Locate every blood parasite and identify its species.
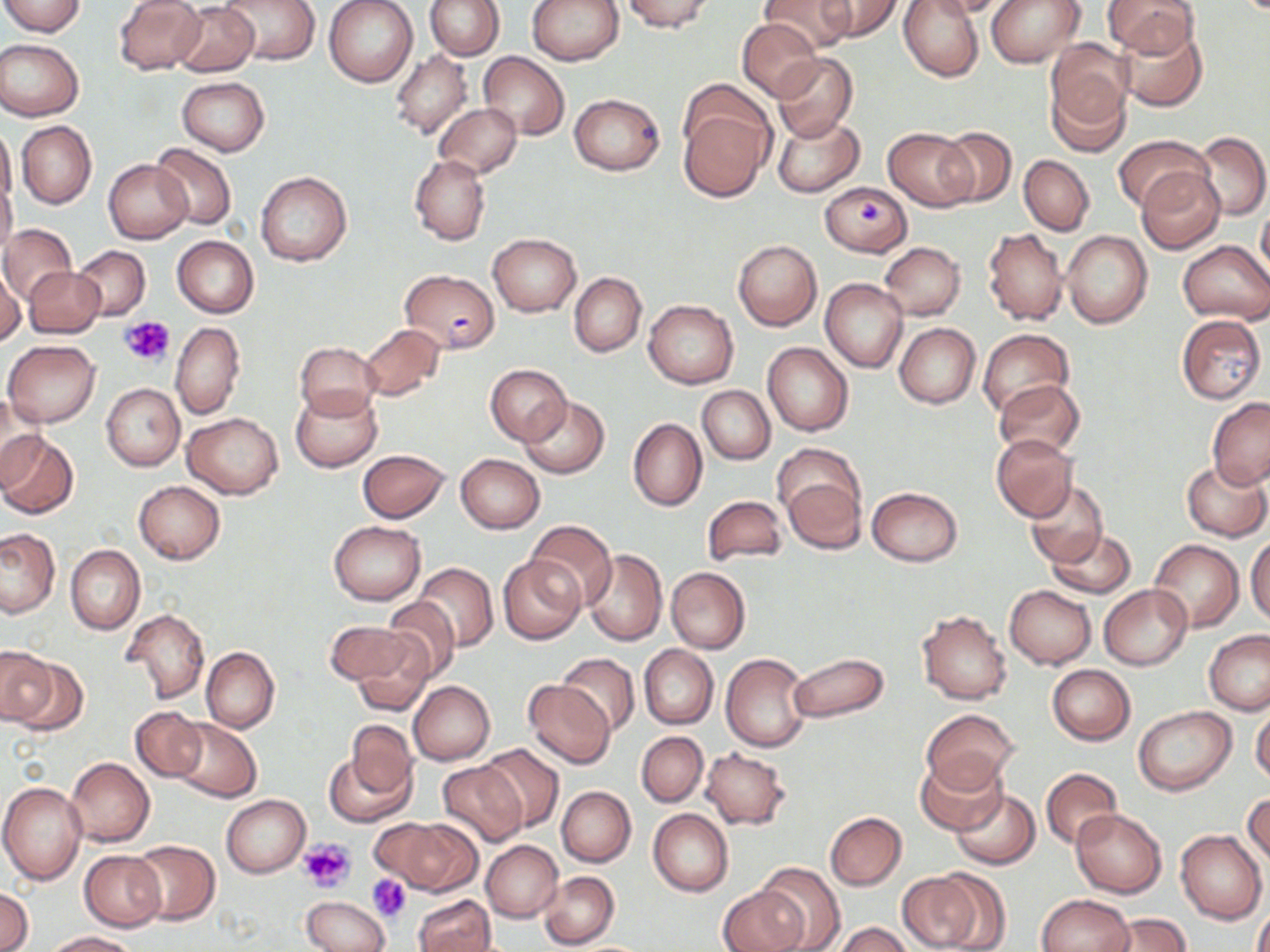

Approximate bounding boxes as (x1, y1, x2, y2) in pixels.
Plasmodium falciparum-infected red blood cells: (400, 269, 500, 354).
No Plasmodium ovale, Plasmodium malariae, Plasmodium vivax, Babesia divergens, or Trypanosoma brucei observed.

Summary:
  - Uninfected red blood cell locations: (2, 0, 86, 36), (219, 0, 321, 65), (324, 0, 418, 87), (425, 0, 504, 60), (527, 0, 624, 65), (621, 0, 715, 33), (758, 0, 857, 55), (817, 0, 902, 42), (898, 0, 985, 81), (923, 0, 1013, 19), (986, 0, 1085, 67), (1104, 0, 1201, 58), (113, 1, 206, 74), (171, 2, 260, 76), (738, 18, 824, 102), (1115, 21, 1207, 111), (0, 39, 83, 121), (1044, 39, 1134, 143), (391, 49, 473, 139), (479, 52, 569, 137), (773, 53, 857, 143), (178, 78, 269, 155), (568, 93, 665, 175), (436, 103, 520, 178), (679, 107, 772, 203), (772, 114, 864, 197), (16, 120, 96, 209), (0, 122, 17, 209), (937, 127, 1016, 206), (885, 128, 976, 210), (1194, 132, 1270, 221), (1113, 134, 1209, 212), (150, 143, 236, 229), (409, 154, 490, 246), (1019, 155, 1094, 235), (104, 160, 191, 244), (1136, 166, 1226, 254), (255, 171, 353, 267), (1, 177, 18, 260), (820, 180, 912, 255), (1258, 204, 1270, 282), (0, 224, 75, 305), (983, 227, 1068, 326), (1061, 231, 1153, 329), (487, 234, 582, 316), (171, 236, 259, 317), (732, 240, 822, 330), (1178, 241, 1270, 323), (880, 242, 965, 320), (72, 246, 150, 318), (1, 265, 25, 344), (25, 267, 104, 337), (569, 273, 646, 356), (820, 279, 908, 372), (644, 299, 739, 388), (1177, 315, 1266, 403), (171, 322, 244, 420), (894, 322, 980, 408), (359, 324, 445, 401), (977, 328, 1074, 420), (3, 340, 101, 426), (295, 342, 380, 418), (762, 342, 853, 436), (486, 364, 571, 445), (994, 380, 1086, 459), (101, 383, 185, 471), (698, 385, 775, 464), (291, 388, 383, 473), (518, 396, 611, 479), (1207, 398, 1270, 488), (0, 400, 49, 490), (182, 412, 283, 499), (628, 417, 707, 511), (0, 431, 78, 519), (991, 434, 1078, 521), (358, 449, 449, 523), (455, 454, 545, 534), (1181, 461, 1269, 540), (780, 470, 866, 553), (133, 480, 224, 564), (1025, 480, 1108, 567), (867, 487, 963, 566), (702, 496, 788, 567), (525, 520, 616, 610), (328, 521, 426, 604), (0, 528, 60, 617), (1044, 528, 1136, 598), (1247, 536, 1270, 627), (1149, 539, 1244, 631), (66, 545, 144, 634), (582, 549, 668, 645), (498, 554, 587, 645), (412, 562, 499, 652), (666, 566, 751, 653), (1099, 584, 1192, 670), (1005, 585, 1095, 669), (381, 596, 461, 683), (123, 608, 210, 703), (917, 610, 1012, 704), (324, 620, 417, 688), (346, 628, 437, 716), (1204, 630, 1270, 716), (638, 645, 717, 729), (0, 646, 56, 726), (202, 647, 278, 732), (557, 652, 640, 736), (720, 652, 812, 753), (787, 652, 889, 723), (1047, 664, 1135, 745), (522, 680, 617, 769), (408, 681, 495, 765), (1250, 701, 1270, 787), (131, 706, 205, 781), (1134, 706, 1235, 795), (923, 709, 1018, 791), (168, 718, 262, 802), (345, 720, 417, 800), (636, 731, 708, 807), (644, 733, 719, 899), (477, 743, 566, 835), (699, 747, 792, 830), (325, 749, 414, 828), (916, 754, 1008, 836), (65, 757, 155, 846), (438, 761, 527, 846), (1041, 768, 1121, 851), (0, 781, 87, 884), (556, 786, 636, 868), (950, 789, 1040, 870), (1244, 790, 1269, 872), (221, 794, 310, 877), (648, 809, 734, 896), (1071, 809, 1167, 897), (824, 811, 907, 890), (380, 817, 481, 894), (1176, 829, 1267, 923), (128, 840, 220, 926), (480, 841, 562, 923), (80, 850, 165, 931), (756, 862, 845, 952), (537, 870, 619, 949), (895, 870, 990, 951), (718, 882, 808, 952), (1, 886, 32, 951), (1037, 893, 1135, 952), (413, 894, 495, 952), (300, 896, 389, 952), (1253, 907, 1270, 952), (1100, 912, 1190, 952), (835, 922, 912, 952), (45, 931, 139, 951)
  - Platelet locations: (119, 316, 176, 367), (299, 838, 356, 892), (367, 873, 413, 921)
  - Slide-level diagnosis: Plasmodium falciparum
  - Preparation: thin blood film
  - Stain: May-Grünwald-Giemsa
  - Image size: 1270×952 pixels
  - Modality: optical microscopy
  - Field of view: one of a larger specimen
  - Magnification: 1000x